Outline each blood parasite and name the species.
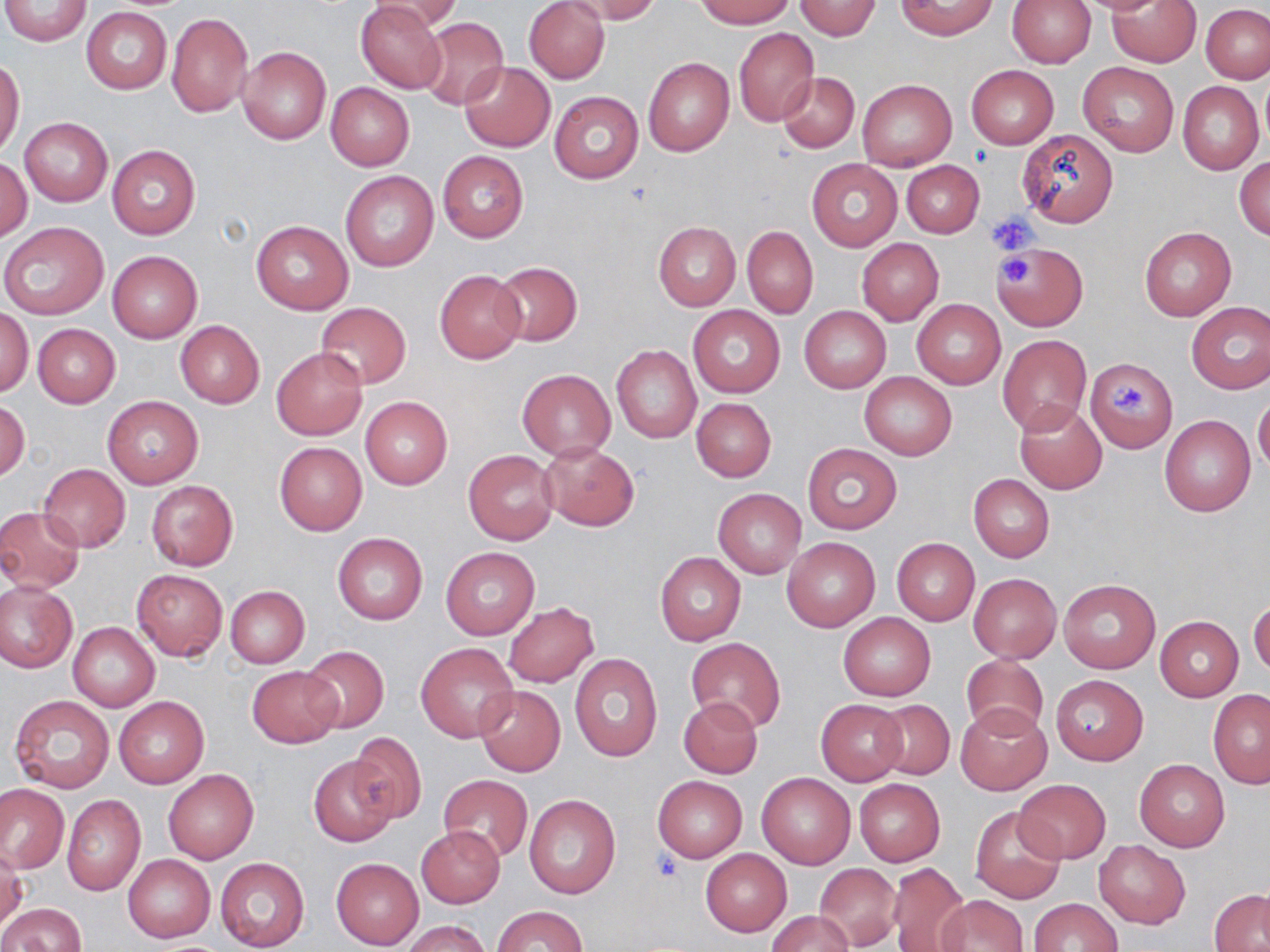
No blood parasites seen.

{
  "slide_level_diagnosis": "no evidence of blood parasites",
  "stain": "May-Grünwald-Giemsa",
  "preparation": "thin blood film",
  "magnification": "1000x",
  "uninfected_red_blood_cell_locations": "approximate bounding boxes as [x1, y1, x2, y2] in pixels: [2, 0, 92, 46], [369, 0, 462, 34], [564, 0, 663, 26], [695, 0, 795, 27], [793, 0, 883, 40], [1071, 0, 1173, 14], [1106, 0, 1202, 67], [355, 1, 447, 95], [523, 1, 610, 83], [895, 1, 997, 39], [1007, 1, 1095, 69], [1201, 4, 1270, 83], [81, 8, 172, 94], [167, 12, 253, 118], [417, 16, 509, 110], [733, 28, 819, 126], [237, 46, 332, 143], [0, 57, 25, 159], [643, 57, 733, 156], [461, 61, 554, 152], [1078, 61, 1178, 156], [966, 65, 1057, 149], [778, 72, 859, 153], [1258, 75, 1270, 153], [857, 79, 957, 170], [1177, 81, 1264, 174], [326, 82, 414, 170], [550, 90, 644, 184], [19, 117, 112, 207], [1018, 129, 1119, 228], [107, 145, 201, 240], [437, 151, 528, 243], [1235, 156, 1270, 241], [1, 158, 33, 241], [807, 159, 902, 250], [901, 160, 985, 238], [340, 171, 440, 272], [251, 219, 353, 314], [0, 221, 110, 321], [653, 222, 740, 310], [742, 226, 817, 318], [1138, 226, 1236, 321], [856, 239, 943, 325], [991, 242, 1088, 330], [108, 250, 201, 343], [491, 262, 582, 346], [434, 270, 526, 362], [911, 298, 1006, 389], [1186, 302, 1270, 394], [314, 303, 412, 388], [1, 306, 33, 399], [687, 306, 786, 398], [799, 306, 891, 392], [176, 321, 264, 408], [32, 323, 121, 407], [996, 334, 1094, 437], [612, 345, 701, 443], [271, 347, 367, 440], [1086, 357, 1177, 453], [517, 368, 617, 461], [860, 372, 957, 460], [103, 394, 204, 487], [1253, 394, 1270, 474], [1, 395, 30, 482], [360, 397, 453, 490], [692, 397, 775, 482], [1014, 400, 1107, 494], [1160, 415, 1256, 516], [273, 441, 367, 535], [539, 442, 639, 531], [803, 443, 901, 535], [463, 450, 558, 545], [39, 464, 130, 551], [968, 473, 1055, 562], [146, 481, 237, 570], [712, 488, 806, 578], [0, 506, 87, 594], [333, 532, 427, 625], [781, 537, 880, 632], [891, 538, 979, 626], [440, 546, 539, 639], [655, 551, 746, 645], [131, 569, 227, 660], [969, 574, 1061, 663], [1058, 580, 1160, 674], [0, 583, 76, 672], [224, 586, 309, 668], [1249, 599, 1270, 676], [503, 601, 599, 686], [838, 612, 935, 700], [1155, 616, 1244, 701], [68, 622, 160, 711], [686, 638, 785, 733], [416, 642, 517, 742], [299, 645, 390, 733], [569, 653, 661, 763], [960, 655, 1048, 740], [247, 666, 343, 747], [1050, 675, 1148, 765], [476, 685, 565, 776], [1208, 691, 1270, 787], [10, 694, 114, 792], [114, 696, 209, 788], [678, 697, 763, 777], [816, 699, 907, 785], [872, 700, 954, 780], [955, 702, 1053, 796], [349, 733, 426, 823], [308, 754, 398, 847], [1134, 759, 1230, 852], [162, 768, 259, 864], [757, 772, 855, 868], [438, 775, 533, 861], [653, 775, 747, 863], [854, 779, 945, 866], [1014, 779, 1110, 864], [0, 783, 68, 873], [524, 794, 621, 899], [62, 795, 144, 895], [971, 807, 1066, 905], [417, 826, 505, 908], [1092, 839, 1190, 929], [0, 846, 26, 931], [701, 849, 791, 935], [122, 853, 215, 943], [215, 858, 309, 952], [331, 858, 424, 949], [886, 862, 968, 952], [815, 863, 901, 949], [1210, 890, 1270, 951], [937, 895, 1028, 952], [1028, 898, 1122, 952], [0, 902, 85, 952], [492, 905, 587, 952], [767, 911, 855, 952], [400, 919, 492, 952]",
  "image_size": "1270×952 pixels",
  "platelet_locations": "approximate bounding boxes as [x1, y1, x2, y2] in pixels: [989, 211, 1038, 255], [1001, 255, 1030, 283], [1112, 383, 1153, 415]",
  "field_of_view": "one of a larger specimen",
  "modality": "light microscopy"
}